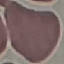

malaria status = uninfected
preparation = thin smear
image type = cell patch, automatically extracted from a larger field of view and resized to 64 × 64 pixels
stain = Giemsa
capture = smartphone through the microscope eyepiece